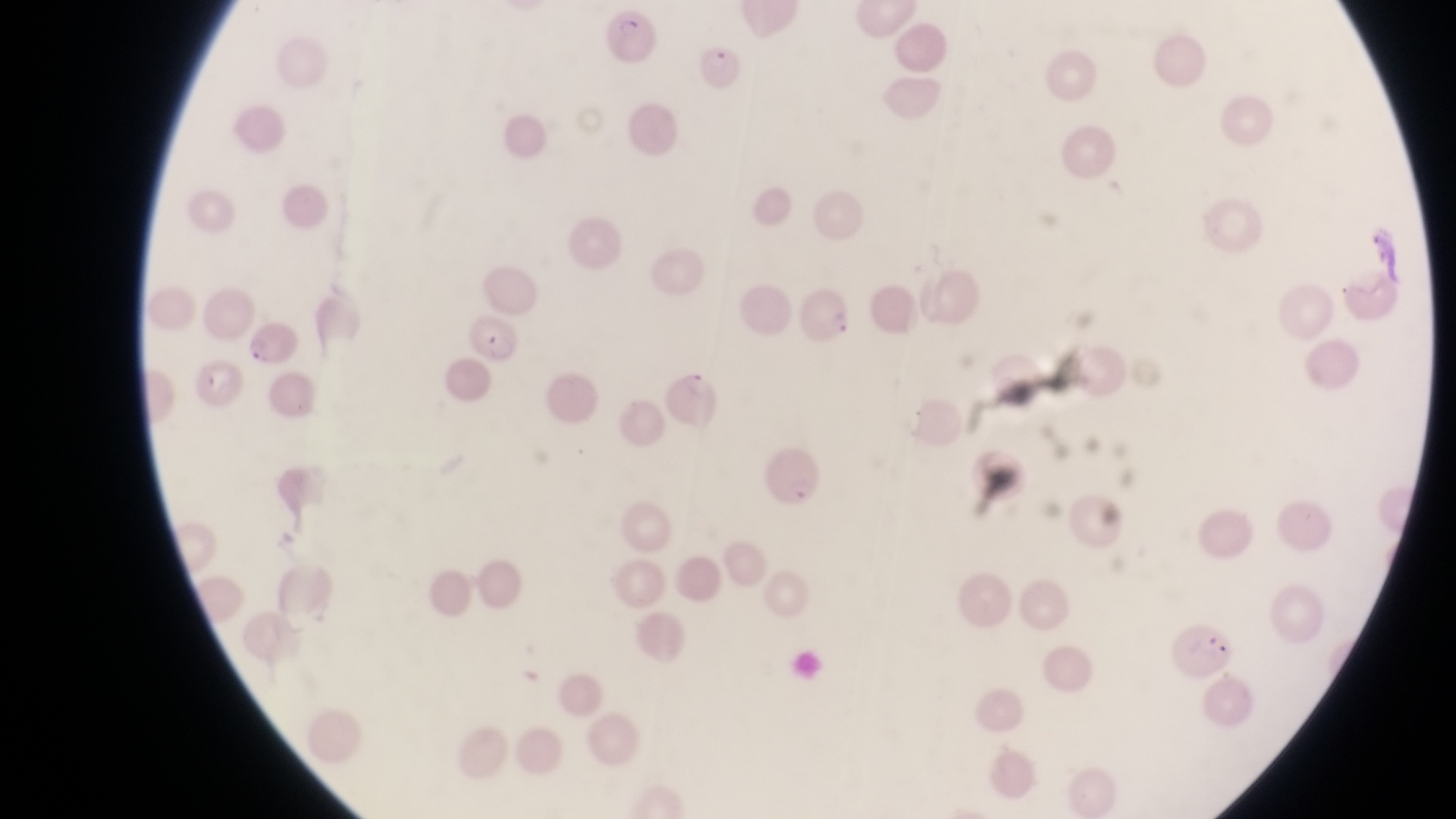

magnification = 1000x
country = Uganda
field of view = single
parasitised red blood cell locations = approximate bounding boxes as [left, top, right, bottom] in pixels: [607, 8, 660, 66], [695, 40, 741, 93], [805, 287, 855, 350], [469, 312, 518, 367], [244, 323, 300, 370], [185, 360, 240, 413], [667, 362, 722, 431], [761, 435, 827, 514], [1168, 618, 1234, 677]
capture = smartphone photograph through the eyepiece of an Olympus CX-23 microscope
image size = 1456×819 pixels
preparation = thin blood film